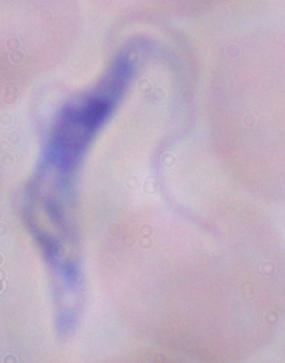

Summary:
  - Magnification: 1000x
  - Modality: photomicrograph
  - Identification: trypanosome